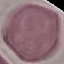
malaria_status: uninfected
preparation: thin blood smear
stain: Giemsa
image_type: automatically extracted cell patch, resized to 64 × 64 pixels
capture: smartphone camera at the microscope eyepiece